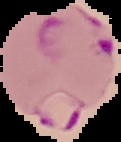
Summary:
  - Malaria status: parasitized
  - Preparation: thin blood film
  - Image type: segmented cell region on a black background
  - Image size: 121×142 pixels